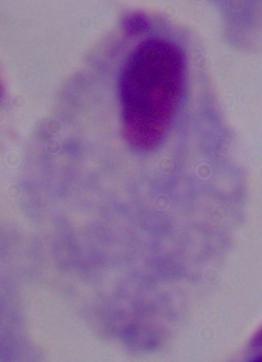
Summary:
  - Modality: micrograph
  - Magnification: 1000x
  - Identification: trichomonad